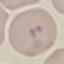
{
  "result": "negative for malaria parasites",
  "image_type": "automatically extracted cell patch, resized to 64 × 64 pixels",
  "stain": "Giemsa",
  "capture": "smartphone camera at the microscope eyepiece",
  "preparation": "thin blood smear"
}